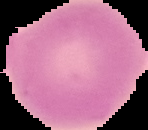
preparation: thin blood film
image_type: segmented cell region with the area outside set to black
result: no malaria parasites detected
image_size: 148×130 pixels